Assess this cell for malaria.
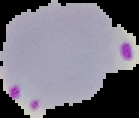
It is parasitized.

image type = segmented cell region with the area outside set to black
image size = 139×118 pixels
preparation = thin blood smear